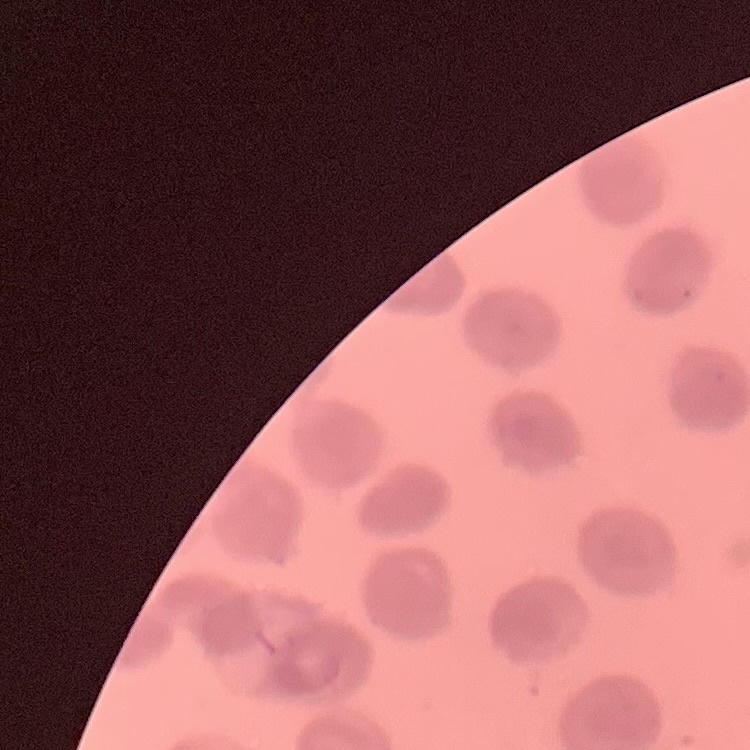
Summary:
  - Erythrocyte morphology: no rouleaux formation
  - Image type: one tile cut from a larger photomicrograph
  - Preparation: thin blood film
  - Stain: Field's or Giemsa